Outline each blood parasite and name the species.
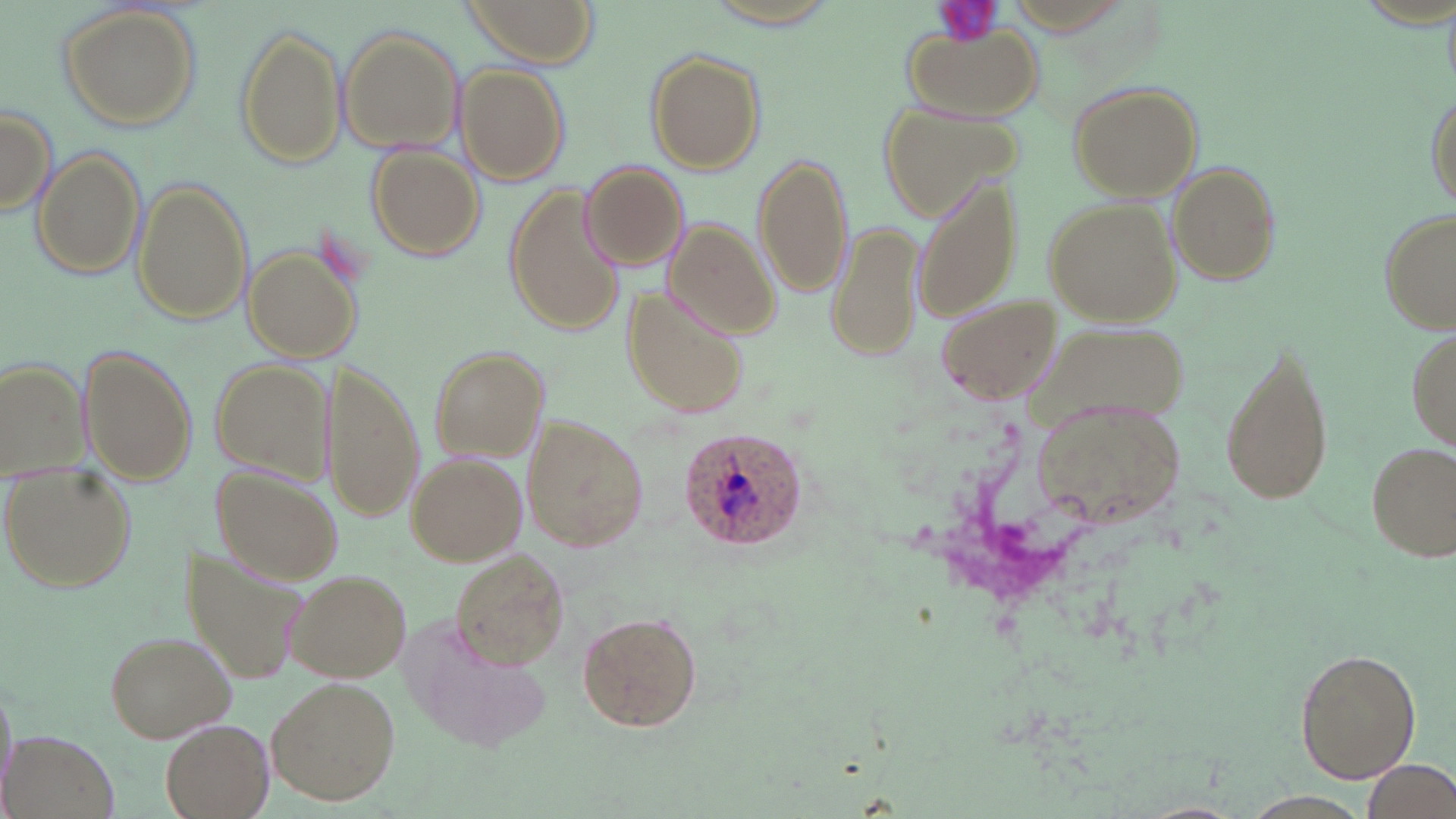

Approximate bounding boxes as [x1, y1, x2, y2] in pixels.
Plasmodium ovale-infected red blood cells: [679, 426, 808, 553].
No Plasmodium falciparum, Plasmodium malariae, Plasmodium vivax, Babesia divergens, or Trypanosoma brucei observed.

Uninfected red blood cell locations: [463, 0, 595, 62], [700, 0, 846, 30], [59, 4, 200, 132], [904, 21, 1040, 120], [235, 24, 347, 170], [338, 24, 465, 152], [644, 47, 766, 175], [457, 62, 572, 185], [1067, 80, 1203, 201], [1425, 87, 1456, 211], [0, 104, 56, 216], [883, 107, 1022, 220], [366, 143, 483, 261], [33, 147, 144, 279], [752, 149, 853, 297], [579, 161, 689, 272], [1170, 163, 1283, 284], [912, 172, 1024, 325], [129, 178, 253, 327], [505, 182, 625, 338], [1044, 197, 1180, 326], [1378, 206, 1455, 339], [829, 215, 922, 365], [663, 219, 780, 339], [243, 242, 363, 365], [621, 288, 746, 421], [937, 294, 1062, 404], [1404, 316, 1456, 460], [1217, 337, 1337, 508], [76, 345, 198, 485], [427, 346, 548, 460], [209, 357, 335, 481], [1, 358, 88, 479], [319, 361, 423, 523], [1031, 396, 1184, 528], [525, 414, 651, 550], [1365, 440, 1454, 563], [406, 452, 525, 566], [1, 466, 135, 593], [213, 467, 342, 586], [183, 545, 310, 687], [450, 547, 573, 669], [287, 568, 411, 683], [578, 610, 703, 732], [409, 623, 556, 754], [104, 629, 237, 742], [1290, 648, 1424, 785], [267, 674, 401, 805], [159, 718, 273, 818], [2, 726, 123, 819], [1360, 760, 1455, 816]. Platelet locations: [932, 0, 1003, 47]. Slide-level diagnosis: Plasmodium ovale. May-Grünwald-Giemsa stain. One field of a larger specimen. Image is 1456×819 pixels. Captured at 1000x magnification. Thin blood film. Optical microscopy.